Point out every Plasmodium parasite and every leukocyte.
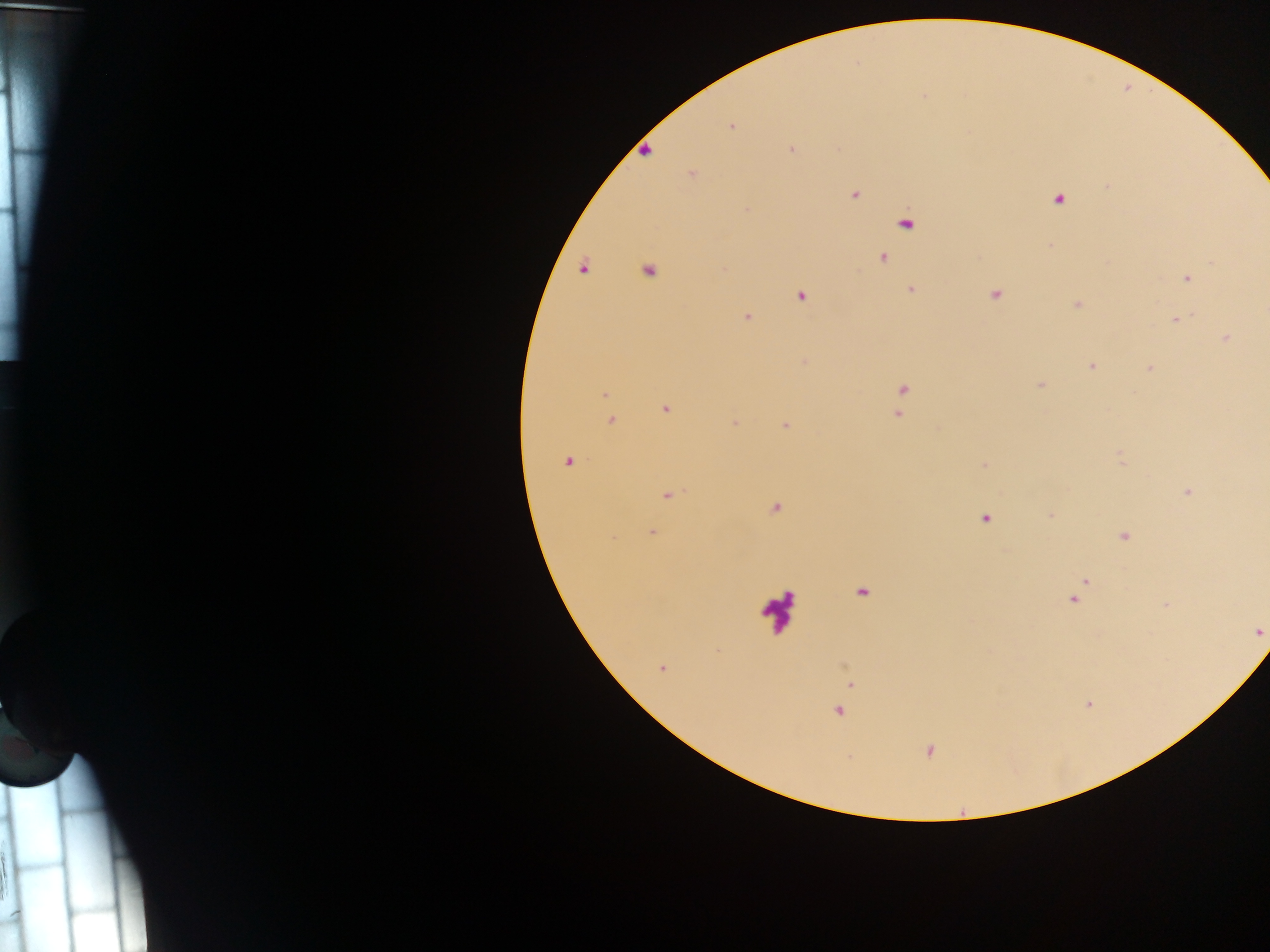
Approximate centers as x y in pixels.
Plasmodium parasites: 923 96; 731 126; 791 150; 645 152; 692 174; 855 194; 1058 200; 748 209; 906 224; 883 257; 1212 261; 584 268; 650 271; 1187 279; 911 289; 995 294; 801 296; 1077 304; 747 318; 1176 320; 1226 338; 1091 366; 1149 368; 1040 385; 902 389; 604 394; 665 409; 897 414; 611 420; 734 423; 786 426; 1121 456; 569 461; 984 465; 1187 491; 667 495; 776 508; 1050 516; 985 518; 652 532; 1123 536; 1084 583; 862 593; 1075 599; 1167 604; 1259 632; 662 667; 852 684; 838 711; 929 750.
Leukocytes: 776 609.

field of view = single
preparation = thick blood smear
image size = 1270×952 pixels
country = Ghana
capture = mobile-phone photograph through a microscope